Identify the parasite.
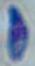

Toxoplasma gondii.

Captured at 1000x magnification. Micrograph.